Name the parasite shown.
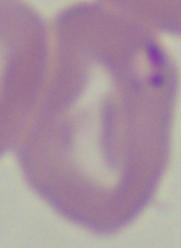
This is Babesia.

Captured at 1000x magnification. Photomicrograph.